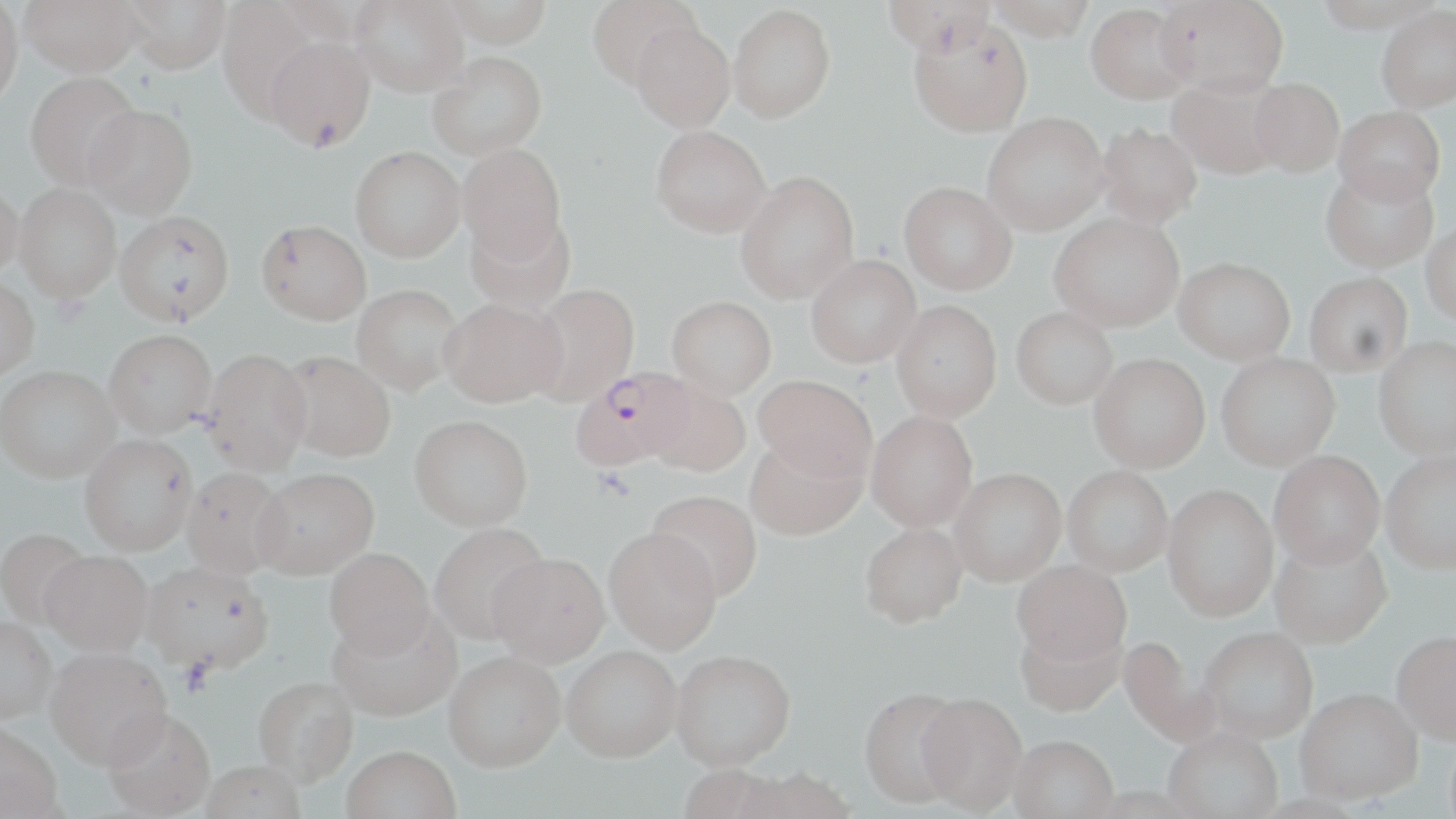
slide_level_diagnosis: Plasmodium falciparum
field_of_view: single
uninfected_red_blood_cell_locations: 'approximate bounding boxes as named x1/y1/x2/y2 corners in pixels: (x1=0, y1=0, x2=24, y2=107), (x1=20, y1=0, x2=144, y2=76), (x1=121, y1=0, x2=231, y2=73), (x1=217, y1=0, x2=326, y2=122), (x1=350, y1=0, x2=469, y2=96), (x1=441, y1=0, x2=553, y2=47), (x1=586, y1=0, x2=700, y2=87), (x1=883, y1=0, x2=995, y2=57), (x1=987, y1=0, x2=1095, y2=41), (x1=1156, y1=0, x2=1289, y2=97), (x1=1311, y1=0, x2=1442, y2=33), (x1=277, y1=1, x2=392, y2=45), (x1=1086, y1=3, x2=1195, y2=104), (x1=728, y1=4, x2=835, y2=122), (x1=1376, y1=5, x2=1456, y2=113), (x1=908, y1=16, x2=1033, y2=137), (x1=630, y1=20, x2=735, y2=132), (x1=264, y1=34, x2=375, y2=152), (x1=427, y1=52, x2=548, y2=160), (x1=25, y1=71, x2=141, y2=191), (x1=1167, y1=76, x2=1286, y2=179), (x1=1249, y1=77, x2=1344, y2=175), (x1=82, y1=103, x2=198, y2=218), (x1=1334, y1=105, x2=1445, y2=206), (x1=982, y1=112, x2=1109, y2=234), (x1=1094, y1=122, x2=1202, y2=229), (x1=651, y1=125, x2=771, y2=237), (x1=458, y1=143, x2=567, y2=263), (x1=350, y1=146, x2=465, y2=262), (x1=1320, y1=167, x2=1438, y2=273), (x1=735, y1=171, x2=859, y2=303), (x1=899, y1=181, x2=1016, y2=294), (x1=0, y1=182, x2=23, y2=283), (x1=13, y1=183, x2=122, y2=304), (x1=113, y1=210, x2=235, y2=327), (x1=1049, y1=212, x2=1184, y2=331), (x1=466, y1=213, x2=576, y2=312), (x1=256, y1=219, x2=371, y2=325), (x1=1420, y1=220, x2=1456, y2=325), (x1=806, y1=254, x2=921, y2=368), (x1=1174, y1=256, x2=1295, y2=364), (x1=1304, y1=272, x2=1412, y2=376), (x1=0, y1=278, x2=39, y2=381), (x1=351, y1=284, x2=463, y2=395), (x1=526, y1=284, x2=640, y2=406), (x1=666, y1=296, x2=777, y2=401), (x1=441, y1=297, x2=566, y2=409), (x1=891, y1=300, x2=1001, y2=423), (x1=1011, y1=307, x2=1117, y2=409), (x1=104, y1=329, x2=216, y2=440), (x1=1373, y1=335, x2=1456, y2=460), (x1=201, y1=349, x2=313, y2=478), (x1=278, y1=351, x2=396, y2=465), (x1=1216, y1=353, x2=1340, y2=470), (x1=1089, y1=354, x2=1210, y2=473), (x1=0, y1=367, x2=120, y2=487), (x1=753, y1=377, x2=876, y2=485), (x1=644, y1=381, x2=751, y2=480), (x1=866, y1=411, x2=977, y2=532), (x1=409, y1=420, x2=533, y2=536), (x1=79, y1=437, x2=197, y2=560), (x1=744, y1=438, x2=868, y2=543), (x1=1381, y1=449, x2=1456, y2=574), (x1=1269, y1=450, x2=1385, y2=568), (x1=1063, y1=466, x2=1173, y2=577), (x1=949, y1=469, x2=1066, y2=587), (x1=180, y1=470, x2=289, y2=583), (x1=251, y1=473, x2=379, y2=585), (x1=1162, y1=484, x2=1278, y2=621), (x1=647, y1=491, x2=762, y2=603), (x1=859, y1=525, x2=967, y2=631), (x1=430, y1=526, x2=550, y2=648), (x1=0, y1=529, x2=93, y2=630), (x1=604, y1=530, x2=721, y2=657), (x1=1269, y1=532, x2=1392, y2=648), (x1=324, y1=552, x2=435, y2=664), (x1=40, y1=554, x2=152, y2=661), (x1=487, y1=558, x2=610, y2=671), (x1=1012, y1=560, x2=1131, y2=667), (x1=140, y1=566, x2=273, y2=681), (x1=328, y1=613, x2=462, y2=726), (x1=0, y1=621, x2=55, y2=728), (x1=1016, y1=623, x2=1125, y2=719), (x1=1199, y1=626, x2=1318, y2=742), (x1=1391, y1=630, x2=1456, y2=745), (x1=1118, y1=634, x2=1222, y2=748), (x1=562, y1=651, x2=681, y2=768), (x1=46, y1=652, x2=172, y2=776), (x1=670, y1=653, x2=796, y2=775), (x1=444, y1=656, x2=565, y2=777), (x1=253, y1=679, x2=358, y2=791), (x1=1295, y1=688, x2=1422, y2=806), (x1=858, y1=691, x2=968, y2=811), (x1=918, y1=696, x2=1027, y2=817), (x1=102, y1=715, x2=216, y2=819), (x1=0, y1=727, x2=62, y2=819), (x1=1163, y1=728, x2=1282, y2=819), (x1=1009, y1=738, x2=1119, y2=819), (x1=341, y1=751, x2=460, y2=819), (x1=199, y1=764, x2=305, y2=819), (x1=677, y1=767, x2=787, y2=819), (x1=733, y1=771, x2=856, y2=819), (x1=1087, y1=786, x2=1204, y2=819), (x1=1252, y1=794, x2=1370, y2=819)'
image_size: 1456×819 pixels
plasmodium_falciparum_infected_red_blood_cell_locations: 'approximate bounding boxes as named x1/y1/x2/y2 corners in pixels: (x1=571, y1=367, x2=696, y2=474)'
modality: optical microscopy
magnification: 1000x
preparation: thin blood smear
stain: May-Grünwald-Giemsa
platelet_locations: 'approximate bounding boxes as named x1/y1/x2/y2 corners in pixels: (x1=593, y1=468, x2=635, y2=503), (x1=178, y1=660, x2=216, y2=697)'